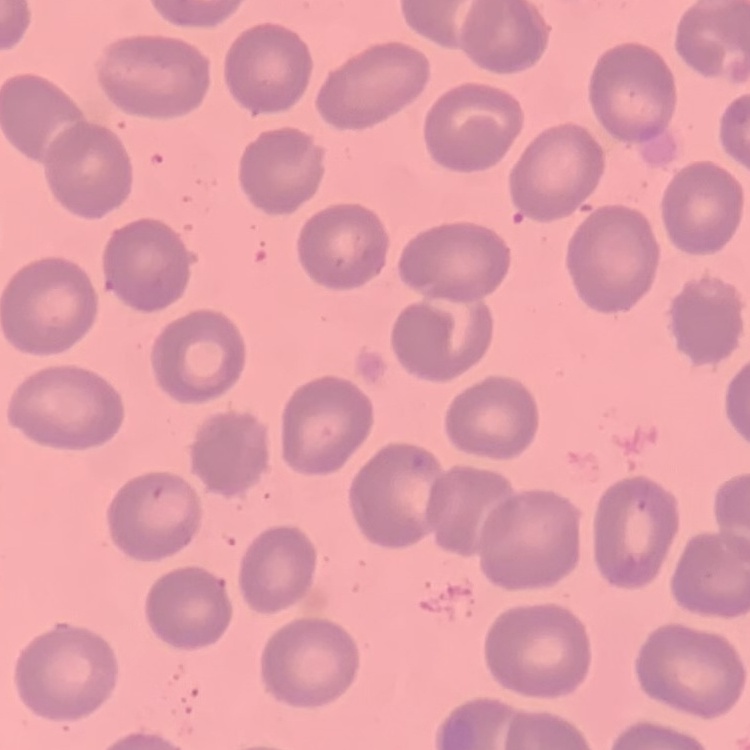
Summary:
  - Erythrocyte morphology: no rouleaux formation
  - Image type: one tile cut from a larger photomicrograph
  - Stain: Field's or Giemsa
  - Preparation: thin blood smear